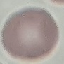

Summary:
  - Malaria status: uninfected
  - Stain: Giemsa
  - Image type: automatically extracted cell patch, resized to 64 × 64 pixels
  - Capture: smartphone camera at the microscope eyepiece
  - Preparation: thin smear